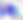
Summary:
  - Modality: micrograph
  - Magnification: 400x
  - Identification: Toxoplasma gondii